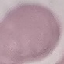
Summary:
  - Result: no malaria parasites seen
  - Image type: automatically extracted cell patch, resized to 64 × 64 pixels
  - Stain: Giemsa
  - Capture: smartphone through the microscope eyepiece
  - Preparation: thin smear